Name the cell type shown.
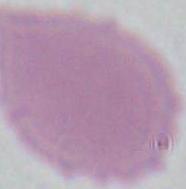
This is an erythrocyte.

Summary:
  - Modality: micrograph
  - Magnification: 1000x